Give the extent of all Plasmodium falciparum-infected red blood cells.
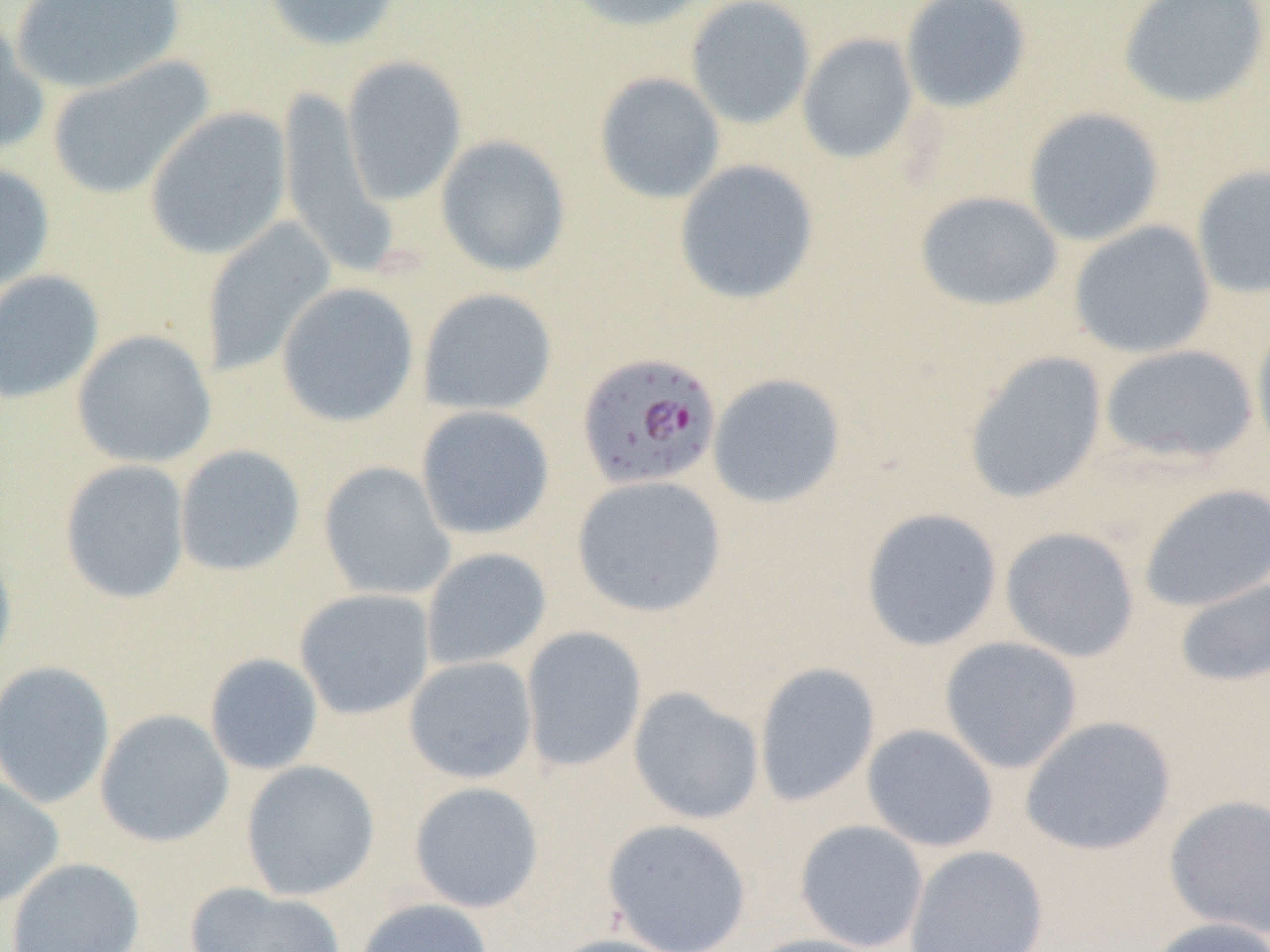
Approximate bounding boxes as (x1,y1)-(x2,y2) corner pairs in pixels.
Plasmodium falciparum-infected red blood cells: (576,350)-(723,492).

Summary:
  - Uninfected red blood cell locations: (10,0)-(186,95), (261,0)-(403,52), (561,0)-(715,33), (685,0)-(817,130), (900,0)-(1033,114), (1117,0)-(1270,110), (0,13)-(49,158), (796,33)-(919,164), (46,56)-(215,201), (341,56)-(467,206), (593,72)-(726,205), (276,84)-(395,278), (144,107)-(293,260), (1023,107)-(1165,247), (435,135)-(571,277), (673,159)-(820,306), (0,162)-(55,297), (1191,164)-(1270,299), (914,191)-(1064,312), (201,217)-(337,379), (1068,220)-(1216,359), (0,269)-(105,405), (275,281)-(420,428), (417,287)-(558,417), (1250,317)-(1270,461), (72,329)-(217,469), (1098,344)-(1259,467), (963,351)-(1108,505), (707,372)-(847,509), (415,405)-(555,540), (174,444)-(306,578), (59,460)-(191,604), (318,461)-(455,601), (571,475)-(727,618), (1137,483)-(1270,612), (860,507)-(1003,652), (1000,526)-(1141,663), (0,535)-(17,683), (421,547)-(552,671), (1174,574)-(1270,689), (294,588)-(435,720), (520,626)-(647,773), (939,636)-(1083,774), (203,653)-(324,775), (403,656)-(538,784), (0,660)-(115,809), (753,662)-(881,808), (627,686)-(765,825), (94,709)-(234,847), (1019,715)-(1177,856), (861,724)-(1000,853), (240,760)-(380,901), (0,777)-(64,910), (408,781)-(545,913), (1165,795)-(1270,939), (601,818)-(753,952), (794,819)-(929,951), (904,845)-(1049,952), (5,856)-(145,951), (184,882)-(348,952), (354,897)-(494,952), (1146,916)-(1270,952), (544,933)-(688,952), (745,933)-(890,952)
  - Slide-level diagnosis: Plasmodium falciparum
  - Field of view: single
  - Modality: light microscopy
  - Image size: 1270×952 pixels
  - Magnification: 1000x
  - Preparation: thin blood smear